Identify the parasite.
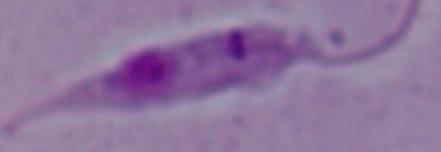

Leishmania.

Summary:
  - Magnification: 1000x
  - Modality: photomicrograph